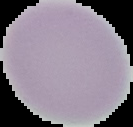
preparation = thin blood smear
image size = 133×127 pixels
result = no Plasmodium parasites seen
image type = segmented cell region with the area outside set to black